Classify this cell by malaria status.
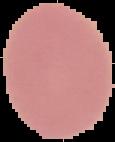

Uninfected.

Summary:
  - Image type: segmented cell region with the area outside set to black
  - Image size: 115×142 pixels
  - Preparation: thin blood film